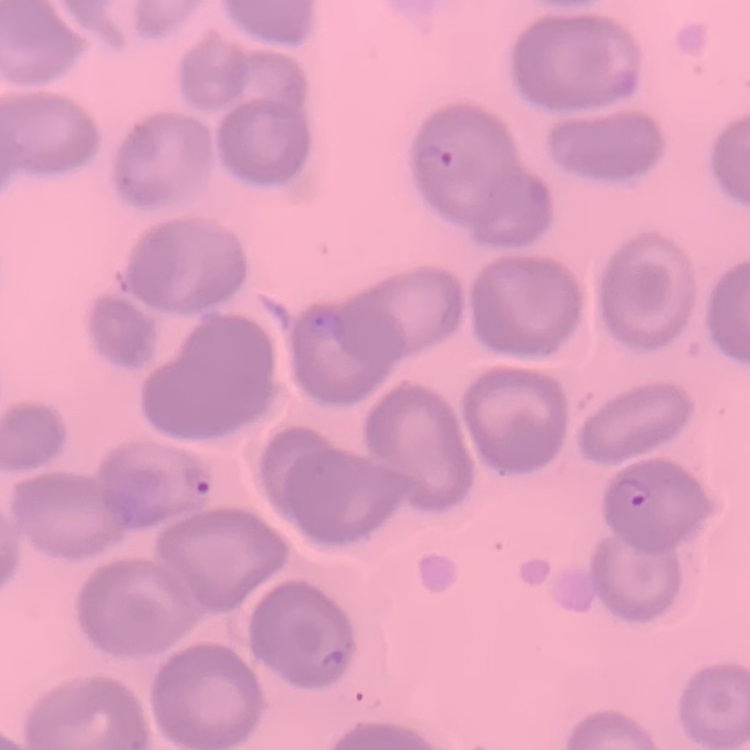

The erythrocytes exhibit no rouleaux formation. Square crop of a larger photomicrograph. Field's or Giemsa stain. Thin blood film.